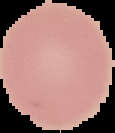

From a thin blood smear. Image is 115×133 pixels. Malaria status: uninfected. Segmented cell region on a black background.